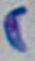 Toxoplasma gondii is seen. Micrograph. Captured at 1000x magnification.